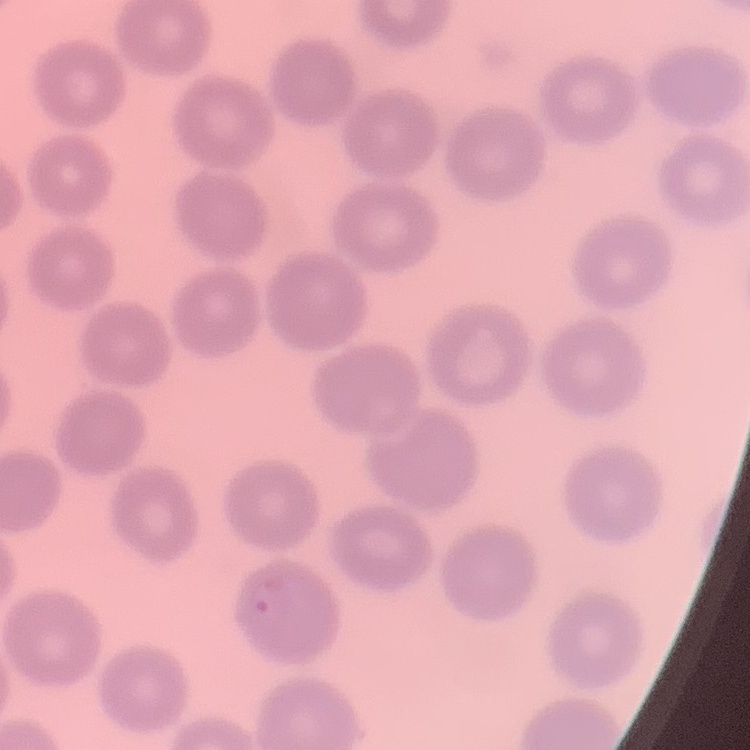

Summary:
  - Red blood cell morphology: no rouleaux formation
  - Image type: square crop of a larger photomicrograph
  - Preparation: thin peripheral smear
  - Stain: Field's or Giemsa